State the blood parasite species.
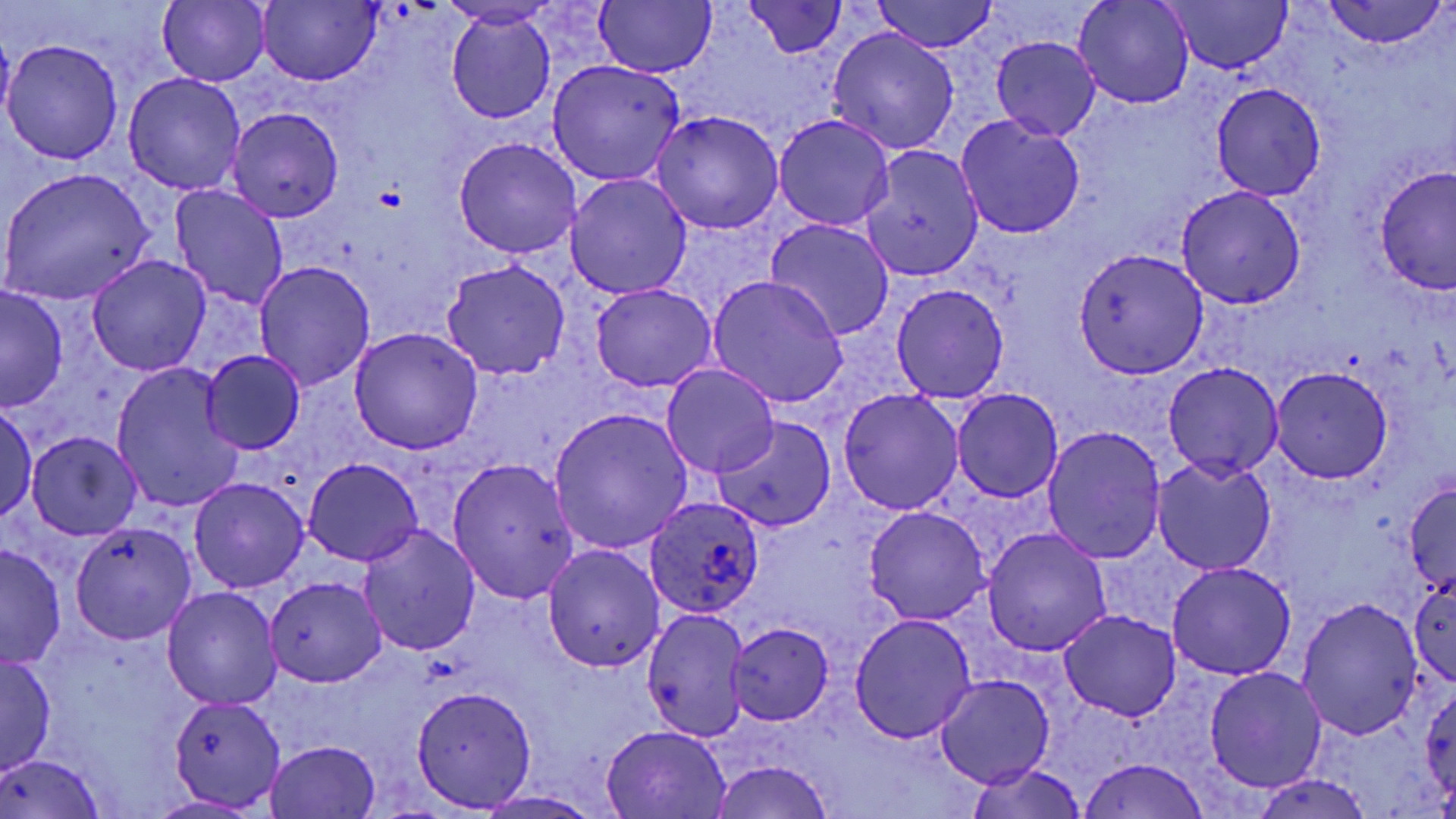
Plasmodium ovale.

Summary:
  - Coordinate format: approximate bounding boxes as named x1/y1/x2/y2 corners in pixels
  - Platelet locations: (x1=375, y1=186, x2=403, y2=211)
  - Uninfected red blood cell locations: (x1=158, y1=0, x2=271, y2=87), (x1=258, y1=0, x2=381, y2=85), (x1=869, y1=0, x2=1001, y2=53), (x1=1074, y1=0, x2=1194, y2=108), (x1=1162, y1=0, x2=1296, y2=73), (x1=594, y1=1, x2=715, y2=78), (x1=1321, y1=1, x2=1447, y2=49), (x1=746, y1=2, x2=849, y2=57), (x1=445, y1=10, x2=556, y2=125), (x1=827, y1=27, x2=959, y2=154), (x1=1, y1=28, x2=16, y2=134), (x1=992, y1=37, x2=1100, y2=139), (x1=3, y1=40, x2=124, y2=164), (x1=546, y1=59, x2=684, y2=185), (x1=124, y1=73, x2=246, y2=195), (x1=1212, y1=84, x2=1326, y2=198), (x1=119, y1=94, x2=342, y2=209), (x1=227, y1=107, x2=346, y2=223), (x1=651, y1=110, x2=783, y2=234), (x1=773, y1=113, x2=894, y2=231), (x1=956, y1=116, x2=1086, y2=238), (x1=452, y1=137, x2=584, y2=259), (x1=859, y1=145, x2=984, y2=281), (x1=1375, y1=166, x2=1455, y2=295), (x1=1, y1=169, x2=155, y2=306), (x1=565, y1=174, x2=691, y2=298), (x1=169, y1=185, x2=290, y2=311), (x1=1176, y1=186, x2=1306, y2=309), (x1=765, y1=218, x2=895, y2=339), (x1=1073, y1=247, x2=1208, y2=377), (x1=88, y1=254, x2=210, y2=375), (x1=441, y1=259, x2=569, y2=380), (x1=254, y1=262, x2=375, y2=392), (x1=706, y1=275, x2=849, y2=409), (x1=589, y1=283, x2=717, y2=391), (x1=890, y1=284, x2=1009, y2=404), (x1=0, y1=288, x2=68, y2=411), (x1=349, y1=328, x2=483, y2=454), (x1=199, y1=350, x2=306, y2=455), (x1=1163, y1=361, x2=1284, y2=480), (x1=662, y1=364, x2=780, y2=477), (x1=110, y1=365, x2=243, y2=513), (x1=1270, y1=366, x2=1394, y2=484), (x1=838, y1=388, x2=963, y2=515), (x1=953, y1=388, x2=1063, y2=502), (x1=0, y1=402, x2=37, y2=522), (x1=548, y1=407, x2=693, y2=556), (x1=712, y1=416, x2=837, y2=533), (x1=1044, y1=425, x2=1168, y2=562), (x1=26, y1=432, x2=141, y2=539), (x1=448, y1=457, x2=580, y2=605), (x1=1152, y1=457, x2=1276, y2=573), (x1=303, y1=459, x2=422, y2=566), (x1=189, y1=476, x2=308, y2=593), (x1=1403, y1=480, x2=1455, y2=595), (x1=864, y1=506, x2=990, y2=625), (x1=70, y1=520, x2=200, y2=644), (x1=357, y1=524, x2=481, y2=656), (x1=982, y1=528, x2=1111, y2=655), (x1=0, y1=542, x2=66, y2=669), (x1=543, y1=545, x2=664, y2=672), (x1=1165, y1=562, x2=1296, y2=680), (x1=1408, y1=573, x2=1455, y2=687), (x1=266, y1=576, x2=386, y2=686), (x1=163, y1=587, x2=282, y2=710), (x1=1296, y1=598, x2=1424, y2=742), (x1=641, y1=607, x2=753, y2=743), (x1=1058, y1=611, x2=1181, y2=723), (x1=850, y1=614, x2=977, y2=743), (x1=726, y1=623, x2=833, y2=726), (x1=0, y1=652, x2=56, y2=775), (x1=1205, y1=667, x2=1326, y2=793), (x1=936, y1=674, x2=1055, y2=788), (x1=1422, y1=684, x2=1456, y2=804), (x1=411, y1=686, x2=537, y2=812), (x1=168, y1=694, x2=288, y2=811), (x1=600, y1=723, x2=732, y2=817), (x1=266, y1=740, x2=380, y2=817), (x1=2, y1=752, x2=103, y2=818), (x1=1076, y1=757, x2=1212, y2=818), (x1=706, y1=761, x2=836, y2=819), (x1=965, y1=762, x2=1088, y2=819), (x1=1252, y1=772, x2=1374, y2=818), (x1=473, y1=792, x2=608, y2=818)
  - Plasmodium ovale-infected red blood cell locations: (x1=646, y1=496, x2=766, y2=620)
  - Image size: 1456×819 pixels
  - Modality: optical microscopy
  - Magnification: 1000x
  - Stain: May-Grünwald-Giemsa
  - Field of view: one of a larger specimen
  - Preparation: thin blood smear